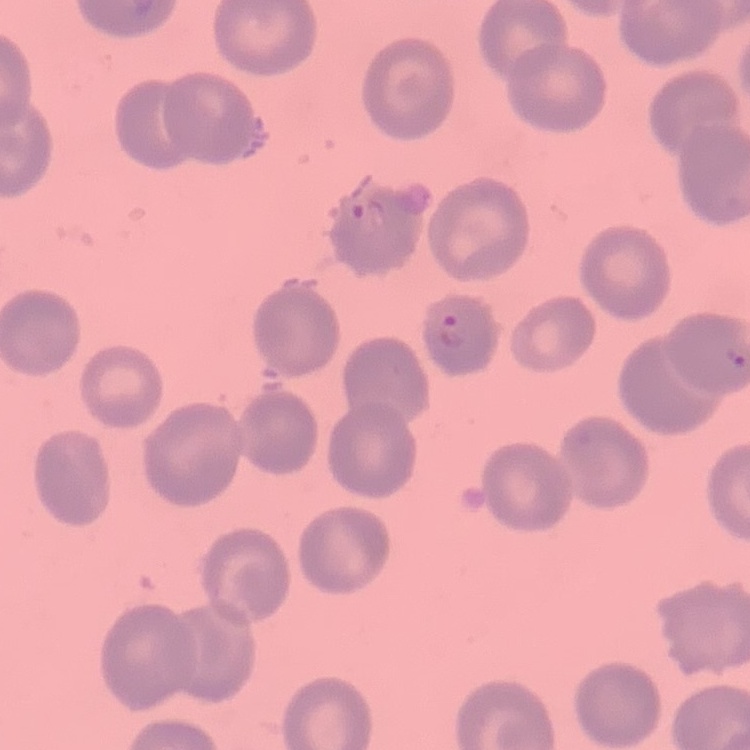

{
  "red_blood_cell_morphology": "no rouleaux formation",
  "image_type": "one tile cut from a larger photomicrograph",
  "stain": "Field's or Giemsa",
  "preparation": "thin blood film"
}